Outline each Plasmodium falciparum-infected red blood cell.
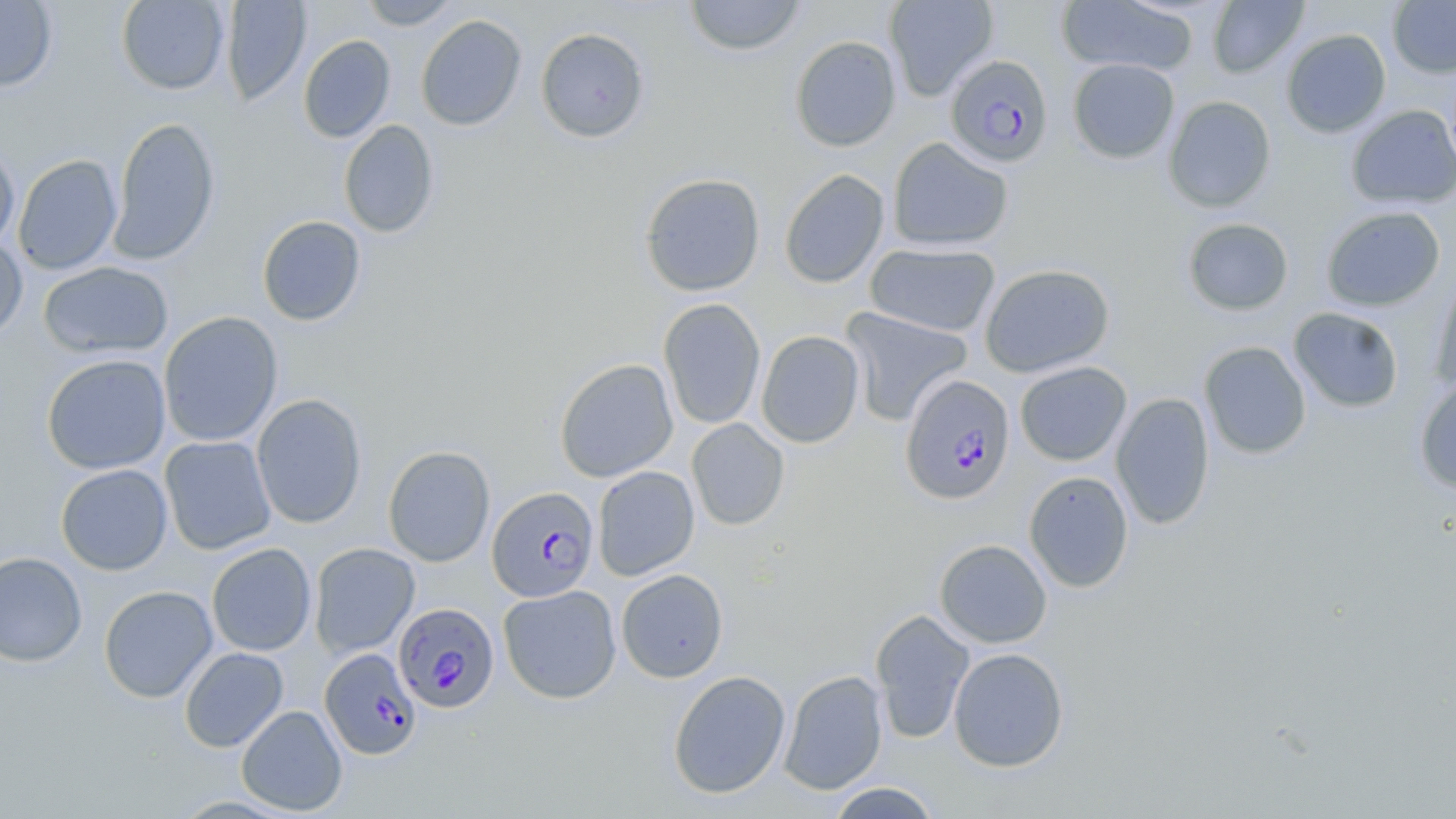

Approximate bounding boxes as (x1,y1)-(x2,y2) corner pairs in pixels.
Plasmodium falciparum-infected red blood cells: (945,54)-(1054,167), (900,374)-(1016,506), (487,486)-(599,602), (393,602)-(499,713), (320,649)-(422,760).

Uninfected red blood cell locations: (116,0)-(230,95), (221,0)-(312,106), (359,0)-(463,30), (684,0)-(806,57), (884,0)-(999,101), (1207,0)-(1308,78), (1388,0)-(1456,78), (0,1)-(58,92), (1056,1)-(1199,77), (416,14)-(527,131), (535,27)-(650,143), (1281,28)-(1392,138), (298,35)-(396,143), (790,35)-(902,151), (1068,58)-(1180,164), (1163,96)-(1276,212), (1345,104)-(1456,210), (108,116)-(220,265), (339,120)-(439,239), (887,137)-(1013,252), (0,139)-(20,253), (13,154)-(122,276), (779,169)-(890,288), (639,172)-(766,297), (1321,206)-(1445,312), (256,215)-(366,326), (1182,218)-(1294,316), (0,233)-(28,342), (865,242)-(1001,337), (38,261)-(174,360), (979,263)-(1115,378), (1431,267)-(1456,393), (658,298)-(766,430), (840,306)-(973,427), (1288,307)-(1404,413), (158,311)-(283,447), (755,330)-(865,448), (1199,341)-(1312,460), (41,354)-(171,474), (555,358)-(678,482), (1014,361)-(1132,466), (1414,378)-(1456,494), (1111,392)-(1215,530), (251,394)-(367,529), (686,418)-(790,531), (159,435)-(277,555), (383,445)-(495,567), (55,464)-(173,575), (593,465)-(699,580), (1023,471)-(1134,593), (934,539)-(1052,648), (309,542)-(420,658), (206,543)-(316,656), (0,551)-(87,667), (616,569)-(729,683), (498,584)-(622,704), (99,585)-(218,703), (869,609)-(976,744), (179,647)-(288,752), (948,648)-(1069,772), (778,669)-(888,795), (668,670)-(791,799), (236,705)-(348,815), (825,782)-(943,818). Slide-level diagnosis: Plasmodium falciparum. Thin blood film. Captured at 1000x magnification. Light microscopy. Image is 1456×819 pixels. May-Grünwald-Giemsa stain. Single field of view.